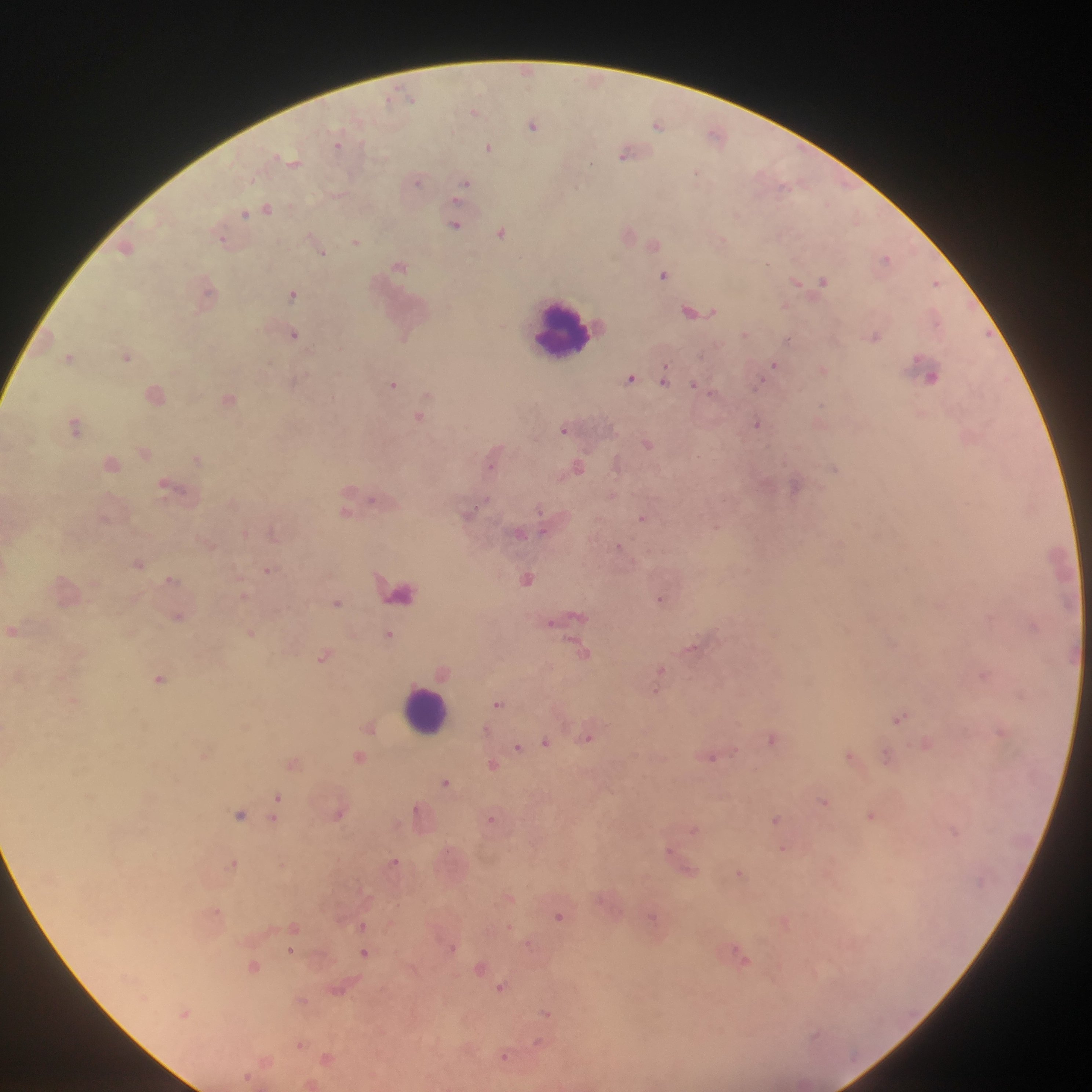

preparation = thick blood film
image size = 1092×1092 pixels
Plasmodium parasite locations = approximate centers as {x, y} in pixels: {526, 71}, {474, 110}, {533, 125}, {659, 125}, {717, 135}, {339, 142}, {489, 146}, {628, 152}, {291, 161}, {418, 179}, {465, 183}, {266, 209}, {454, 224}, {502, 232}, {629, 234}, {224, 239}, {356, 241}, {654, 243}, {127, 247}, {319, 247}, {886, 259}, {399, 266}, {664, 275}, {822, 281}, {937, 283}, {208, 291}, {293, 293}, {786, 305}, {696, 310}, {294, 334}, {746, 334}, {874, 336}, {789, 339}, {127, 355}, {71, 357}, {775, 365}, {823, 368}, {932, 375}, {631, 378}, {665, 379}, {297, 382}, {393, 384}, {694, 384}, {155, 393}, {229, 398}, {420, 415}, {821, 417}, {758, 423}, {75, 424}, {566, 429}, {971, 434}, {648, 443}, {144, 450}, {495, 457}, {198, 459}, {111, 461}, {618, 464}, {577, 466}, {835, 467}, {796, 485}, {173, 487}, {356, 500}, {348, 510}, {469, 512}, {644, 518}, {543, 527}, {273, 531}, {245, 533}, {519, 533}, {209, 543}, {619, 547}, {139, 562}, {270, 569}, {528, 577}, {172, 580}, {66, 589}, {402, 591}, {245, 596}, {662, 598}, {337, 602}, {178, 616}, {569, 616}, {1034, 624}, {12, 630}, {251, 632}, {390, 634}, {692, 647}, {583, 652}, {325, 656}, {442, 669}, {661, 673}, {984, 674}, {161, 678}, {658, 685}, {74, 700}, {498, 703}, {900, 716}, {370, 726}, {487, 729}, {1002, 732}, {588, 736}, {773, 738}, {546, 742}, {927, 743}, {518, 746}, {203, 755}, {852, 755}, {888, 756}, {359, 757}, {712, 757}, {294, 762}, {494, 764}, {447, 781}, {277, 798}, {825, 801}, {339, 812}, {241, 814}, {420, 814}, {872, 815}, {274, 819}, {492, 819}, {777, 819}, {694, 828}, {784, 849}, {394, 862}, {681, 862}, {234, 863}, {740, 872}, {509, 897}, {216, 911}, {560, 916}, {654, 917}, {785, 922}, {363, 925}, {294, 926}, {509, 927}, {530, 943}, {452, 946}, {291, 950}, {365, 952}, {741, 956}, {255, 966}, {482, 966}, {502, 986}, {340, 988}, {302, 1000}, {186, 1012}, {548, 1014}, {300, 1043}, {505, 1056}, {327, 1057}, {266, 1060}, {248, 1077}, {312, 1084}
capture = mobile-phone photograph through a microscope
leukocyte locations = approximate centers as {x, y} in pixels: {561, 329}, {426, 711}
country = Ghana
field of view = single